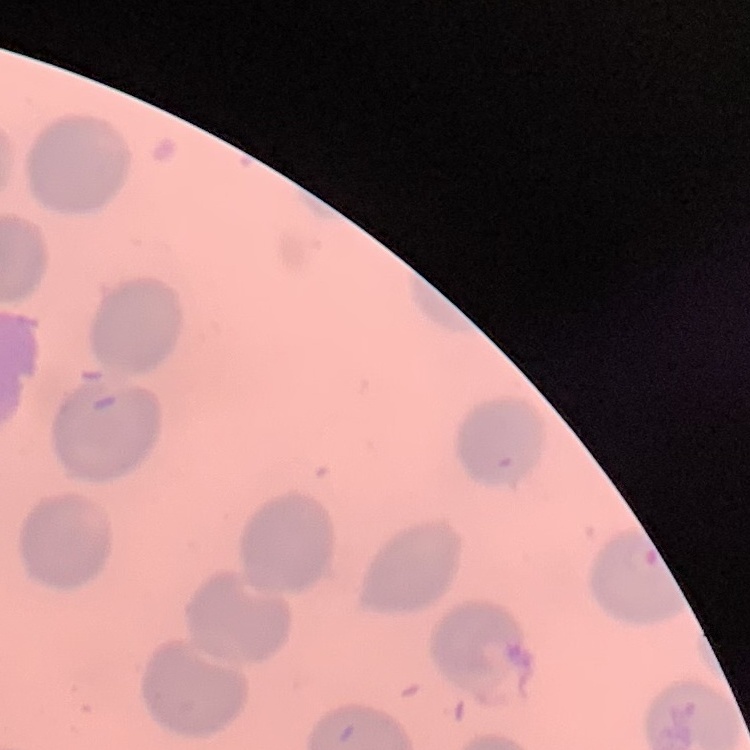

The erythrocytes exhibit no rouleaux formation. Square crop of a larger photomicrograph. Field's or Giemsa stain. Thin peripheral smear.